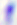
Summary:
  - Magnification: 400x
  - Identification: Toxoplasma gondii
  - Modality: micrograph